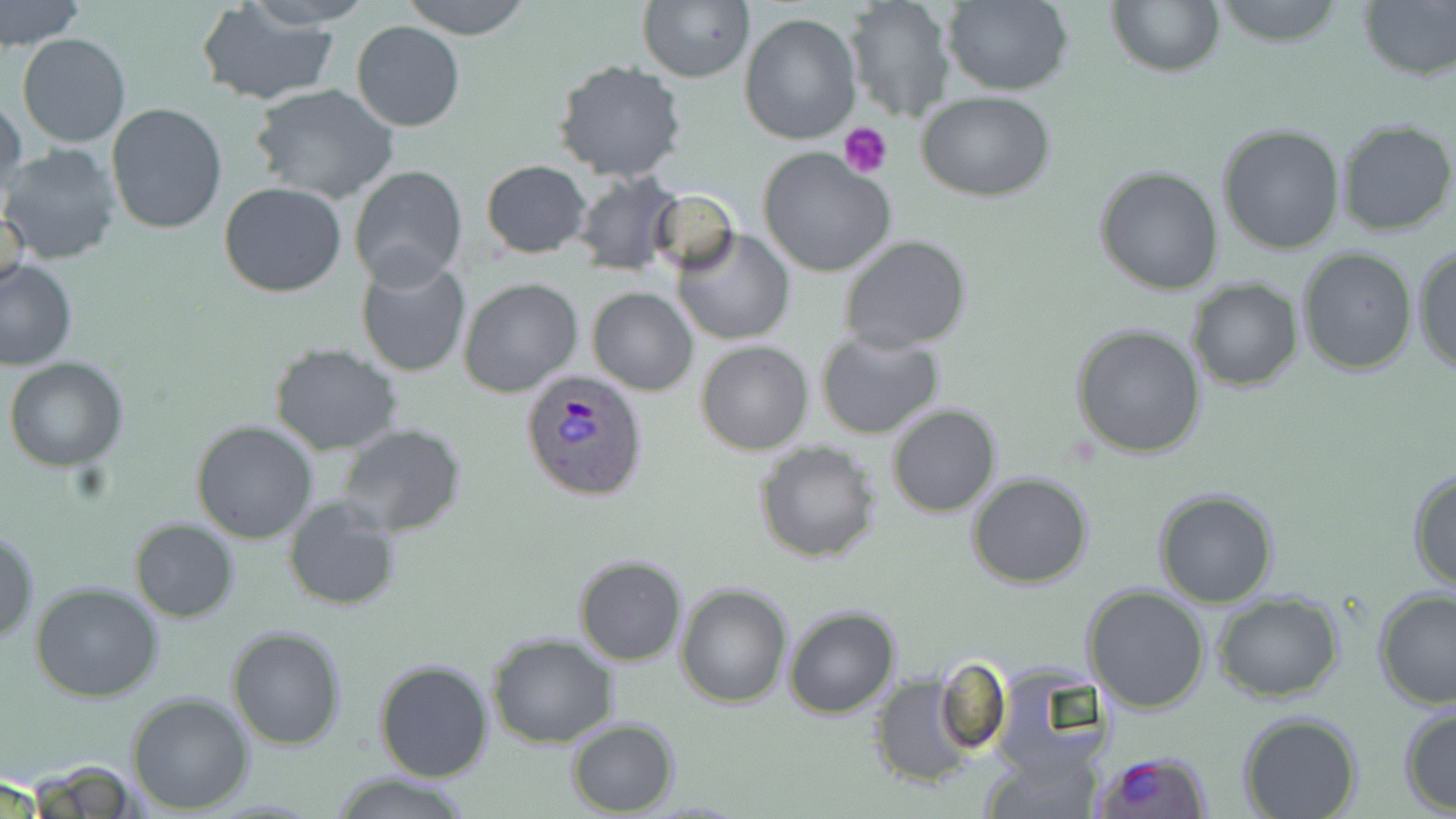

Summary:
  - Coordinate format: approximate bounding boxes as (x1,y1)-(x2,y2) corner pairs in pixels
  - Uninfected red blood cell locations: (0,0)-(85,51), (240,0)-(377,29), (398,0)-(532,38), (944,0)-(1073,96), (1108,0)-(1223,76), (1208,0)-(1350,49), (1357,0)-(1455,81), (638,1)-(754,82), (843,1)-(953,122), (195,2)-(342,107), (640,2)-(835,105), (738,11)-(861,144), (352,20)-(465,131), (19,34)-(131,148), (553,59)-(687,183), (250,85)-(401,204), (916,91)-(1057,203), (1,92)-(25,212), (106,103)-(230,235), (1334,118)-(1456,239), (1218,124)-(1347,254), (2,143)-(122,264), (756,148)-(897,280), (481,160)-(592,257), (349,164)-(469,288), (1094,166)-(1224,296), (569,171)-(684,278), (219,182)-(347,297), (648,189)-(741,274), (0,199)-(29,302), (672,229)-(796,346), (839,236)-(972,354), (1412,244)-(1455,378), (1296,245)-(1418,375), (354,256)-(472,376), (1,258)-(77,371), (458,278)-(583,397), (1188,279)-(1302,390), (587,287)-(697,396), (1070,325)-(1207,460), (815,329)-(945,440), (695,340)-(813,456), (270,344)-(403,455), (7,358)-(128,471), (886,404)-(1000,517), (190,419)-(319,543), (336,423)-(466,537), (754,441)-(882,563), (1407,467)-(1456,593), (966,470)-(1096,589), (1154,489)-(1279,607), (282,499)-(403,611), (130,518)-(238,621), (0,527)-(38,646), (573,554)-(687,667), (29,581)-(162,702), (676,582)-(792,708), (1086,584)-(1212,715), (510,586)-(641,727), (1372,588)-(1456,712), (1212,591)-(1344,702), (783,605)-(902,719), (226,626)-(346,750), (488,633)-(618,748), (372,659)-(494,782), (935,659)-(1011,757), (870,676)-(982,789), (126,691)-(254,812), (1398,703)-(1456,815), (1238,712)-(1364,819), (566,717)-(679,816), (980,737)-(1101,818), (24,762)-(147,818), (325,771)-(480,819)
  - Platelet locations: (840,124)-(894,178)
  - Plasmodium ovale-infected red blood cell locations: (518,368)-(650,504), (1091,749)-(1215,818)
  - Slide-level diagnosis: Plasmodium ovale
  - Modality: optical microscopy
  - Preparation: thin blood film
  - Magnification: 1000x
  - Field of view: single
  - Image size: 1456×819 pixels
  - Stain: May-Grünwald-Giemsa